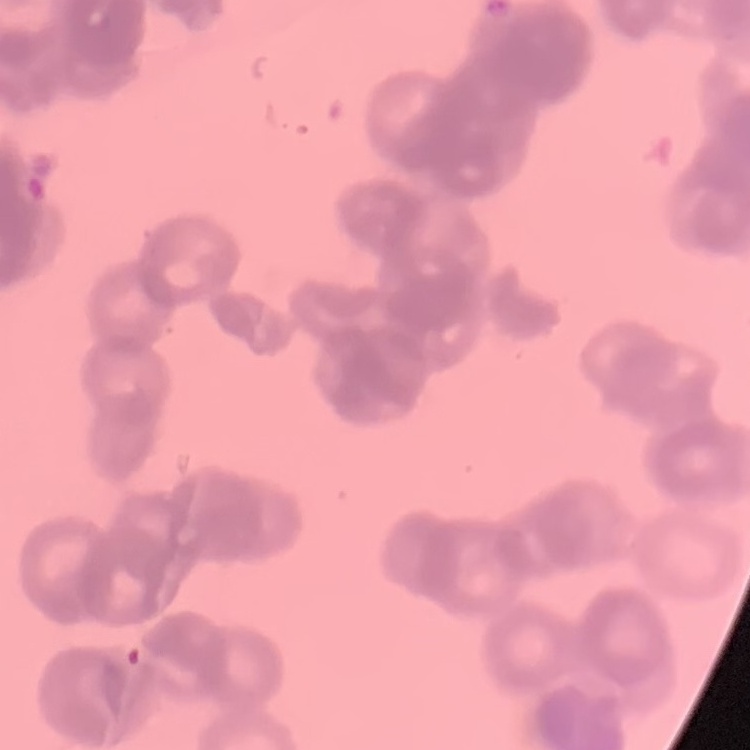
erythrocyte morphology = rouleaux formation
stain = Field's or Giemsa
image type = one tile cut from a larger photomicrograph
preparation = thin peripheral smear